Describe the morphology of the erythrocytes.
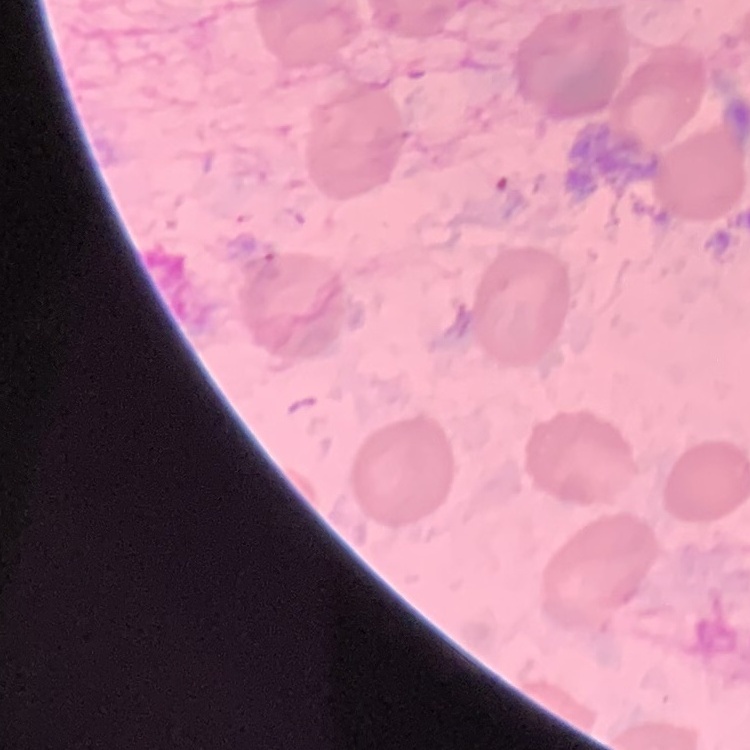
They show no rouleaux formation.

Summary:
  - Stain: Field's or Giemsa
  - Preparation: thin blood smear
  - Image type: one tile cut from a larger photomicrograph